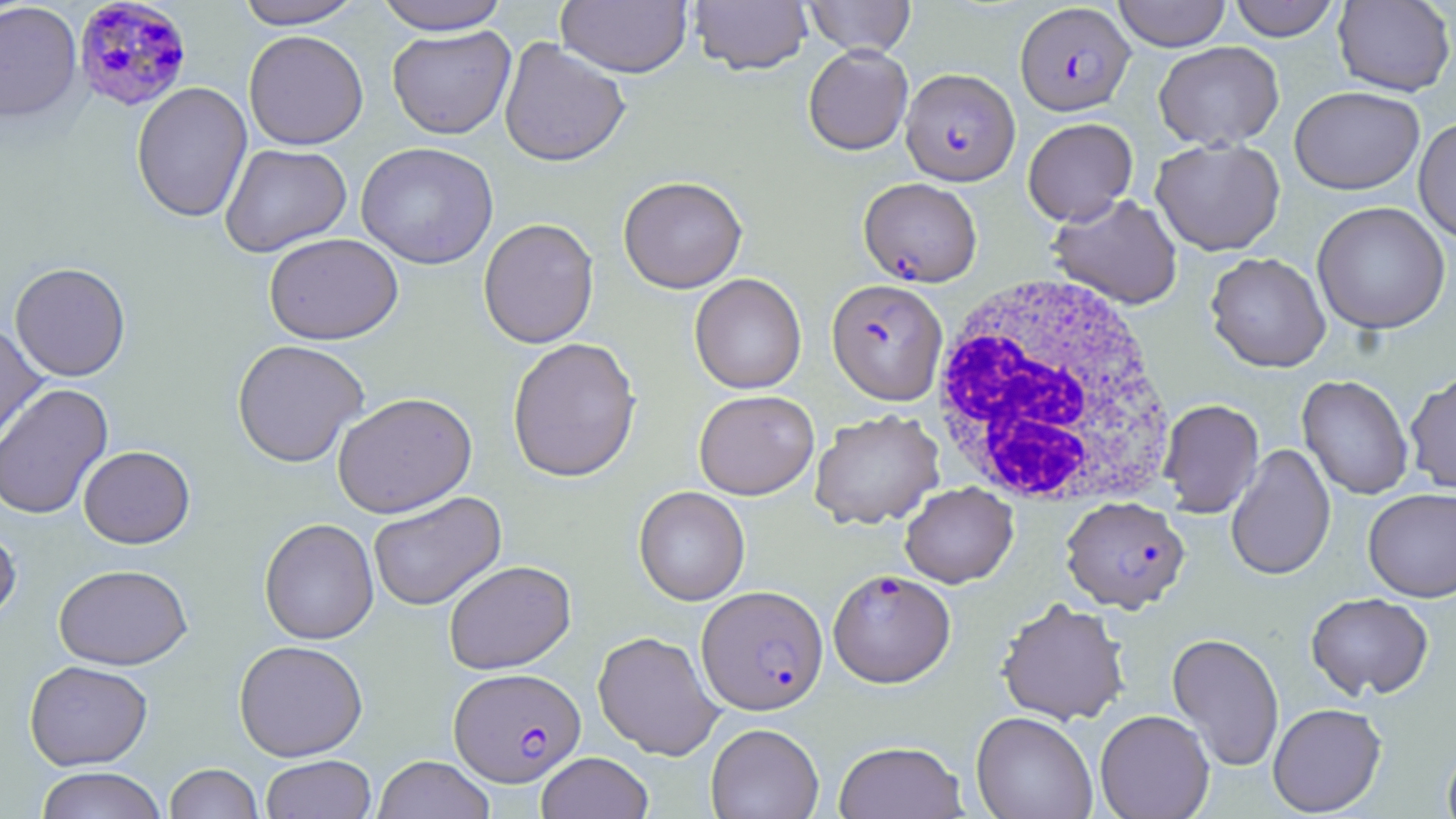
Approximate bounding boxes as named x1/y1/x2/y2 corners in pixels. Uninfected red blood cell locations: (x1=233, y1=0, x2=366, y2=29), (x1=371, y1=0, x2=513, y2=34), (x1=689, y1=0, x2=813, y2=75), (x1=803, y1=0, x2=916, y2=57), (x1=1111, y1=0, x2=1232, y2=51), (x1=1227, y1=0, x2=1341, y2=41), (x1=556, y1=1, x2=692, y2=77), (x1=1333, y1=1, x2=1455, y2=96), (x1=0, y1=2, x2=82, y2=123), (x1=387, y1=25, x2=516, y2=139), (x1=243, y1=30, x2=368, y2=150), (x1=499, y1=37, x2=630, y2=167), (x1=1154, y1=41, x2=1284, y2=150), (x1=803, y1=45, x2=913, y2=156), (x1=132, y1=81, x2=252, y2=223), (x1=1289, y1=86, x2=1425, y2=195), (x1=1413, y1=116, x2=1456, y2=245), (x1=1023, y1=117, x2=1138, y2=225), (x1=1151, y1=137, x2=1286, y2=255), (x1=356, y1=142, x2=499, y2=269), (x1=219, y1=143, x2=352, y2=257), (x1=618, y1=175, x2=747, y2=294), (x1=1047, y1=193, x2=1183, y2=309), (x1=1312, y1=202, x2=1451, y2=334), (x1=478, y1=217, x2=599, y2=349), (x1=264, y1=232, x2=403, y2=344), (x1=1205, y1=252, x2=1331, y2=372), (x1=9, y1=262, x2=130, y2=381), (x1=689, y1=273, x2=807, y2=394), (x1=0, y1=319, x2=47, y2=452), (x1=506, y1=336, x2=641, y2=483), (x1=232, y1=339, x2=369, y2=467), (x1=1404, y1=370, x2=1456, y2=496), (x1=1297, y1=375, x2=1414, y2=500), (x1=0, y1=383, x2=114, y2=520), (x1=694, y1=389, x2=819, y2=499), (x1=332, y1=391, x2=477, y2=518), (x1=1159, y1=399, x2=1264, y2=517), (x1=809, y1=410, x2=945, y2=529), (x1=1225, y1=443, x2=1336, y2=581), (x1=79, y1=445, x2=195, y2=548), (x1=899, y1=482, x2=1018, y2=588), (x1=634, y1=486, x2=750, y2=606), (x1=1363, y1=487, x2=1456, y2=601), (x1=367, y1=491, x2=506, y2=612), (x1=259, y1=518, x2=379, y2=645), (x1=0, y1=521, x2=21, y2=625), (x1=444, y1=559, x2=576, y2=674), (x1=54, y1=564, x2=193, y2=670), (x1=1306, y1=592, x2=1434, y2=700), (x1=997, y1=598, x2=1130, y2=726), (x1=592, y1=631, x2=723, y2=759), (x1=1167, y1=632, x2=1285, y2=772), (x1=233, y1=640, x2=368, y2=761), (x1=24, y1=660, x2=153, y2=770), (x1=1268, y1=703, x2=1386, y2=816), (x1=1095, y1=709, x2=1214, y2=819), (x1=971, y1=711, x2=1097, y2=819), (x1=705, y1=722, x2=824, y2=818), (x1=833, y1=740, x2=968, y2=819), (x1=1442, y1=743, x2=1456, y2=819), (x1=536, y1=752, x2=653, y2=819), (x1=260, y1=754, x2=376, y2=818), (x1=373, y1=755, x2=495, y2=819), (x1=164, y1=763, x2=263, y2=819), (x1=35, y1=767, x2=167, y2=819). White blood cell locations: (x1=930, y1=274, x2=1174, y2=510). Plasmodium falciparum-infected red blood cell locations: (x1=72, y1=0, x2=193, y2=113), (x1=1015, y1=2, x2=1134, y2=115), (x1=901, y1=68, x2=1019, y2=185), (x1=858, y1=177, x2=983, y2=287), (x1=827, y1=278, x2=947, y2=404), (x1=1061, y1=496, x2=1190, y2=613), (x1=828, y1=569, x2=956, y2=688), (x1=697, y1=585, x2=827, y2=715), (x1=449, y1=667, x2=585, y2=786). Slide-level diagnosis: Plasmodium falciparum. May-Grünwald-Giemsa stain. Captured at 1000x magnification. Optical microscopy. Thin blood smear. Single field of view. Image is 1456×819 pixels.